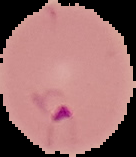

From a thin blood film. Cell region segmented out of the field of view; the surrounding area is masked to black. Malaria status: parasitized. Image is 136×157 pixels.